Give the preparation type.
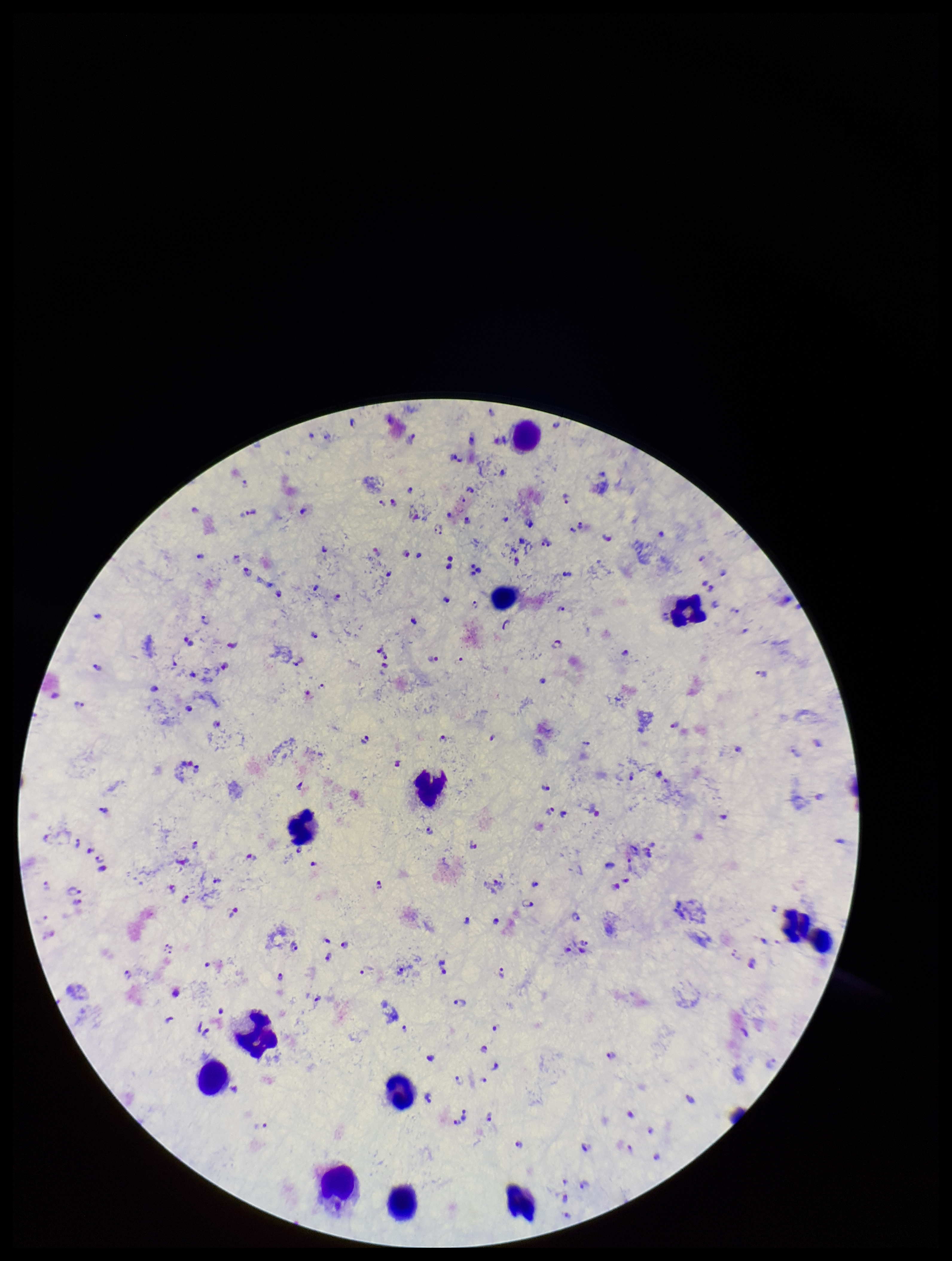
Thick.

Summary:
  - Patient malaria status: infected
  - Species reported for this patient: Plasmodium falciparum
  - Capture: smartphone photograph through the microscope eyepiece
  - Parasite count: 227
  - Plasmodium parasites: identified
  - Stain: Giemsa
  - Leukocyte count: 13
  - Image size: 952×1261 pixels
  - Field of view: one from this slide